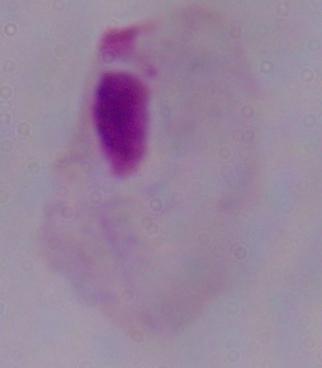

modality = micrograph
identification = trichomonad
magnification = 1000x